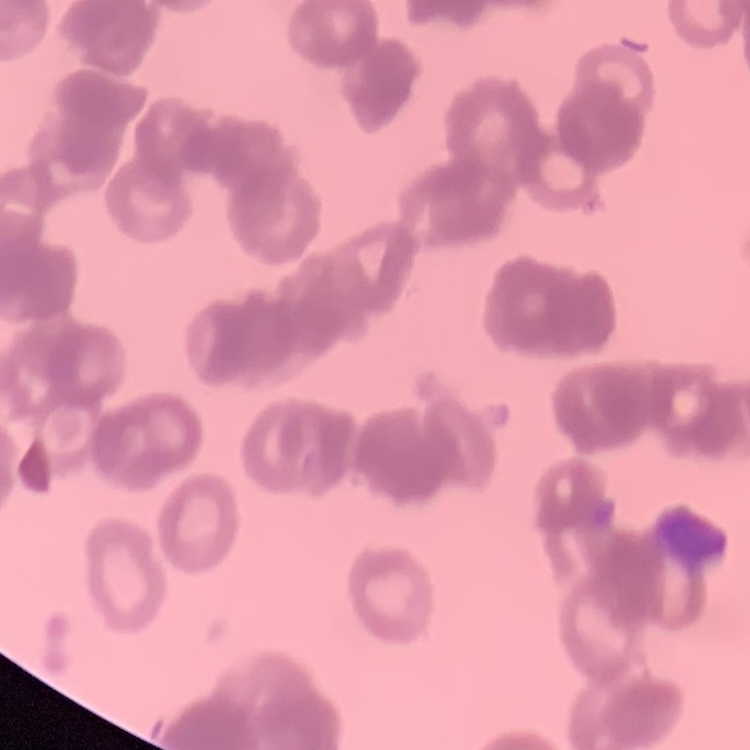

{
  "red_blood_cell_morphology": "rouleaux formation",
  "image_type": "one tile cut from a larger photomicrograph",
  "preparation": "thin blood smear",
  "stain": "Field's or Giemsa"
}